Give the position of every malaria parasite.
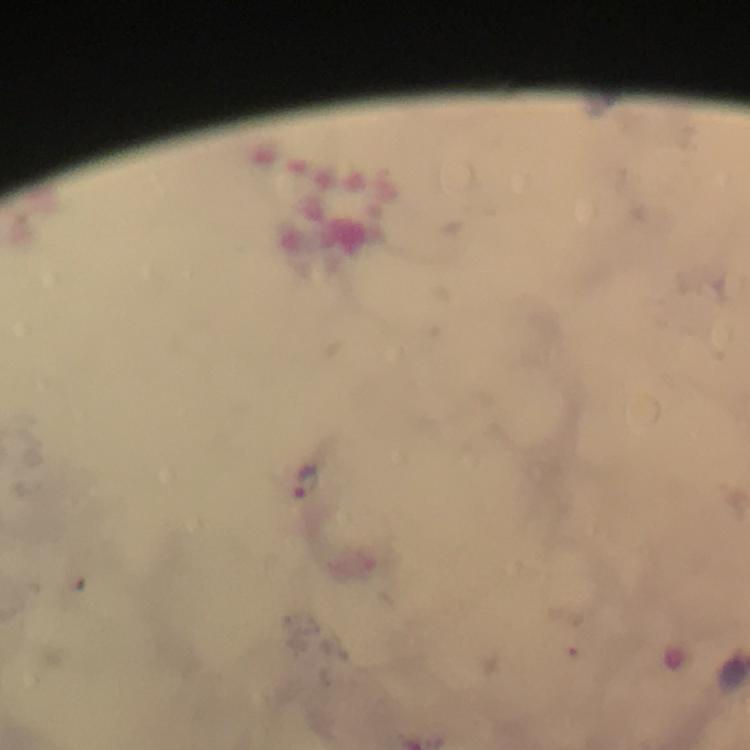
Approximate object centers, in pixels from the top-left corner.
Malaria parasites: (x=305, y=484).

A crop from one field of view. At 100x magnification. Image is 750×750 pixels. Immersion oil applied. Smartphone photograph taken through a microscope. From a diagnostic examination for malaria. Thick smear. Giemsa-stained preparation.